Identify the parasite.
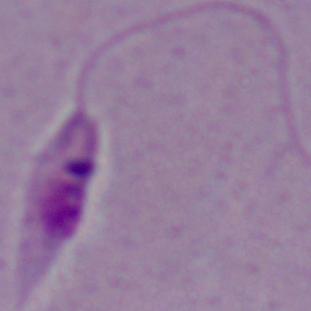
Leishmania.

Photomicrograph. Captured at 1000x magnification.